Assess this cell for malaria.
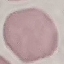

Uninfected.

Summary:
  - Stain: Giemsa
  - Preparation: thin smear
  - Image type: cell patch, automatically extracted from a larger field of view and resized to 64 × 64 pixels
  - Capture: smartphone through the microscope eyepiece